Evaluate for malaria.
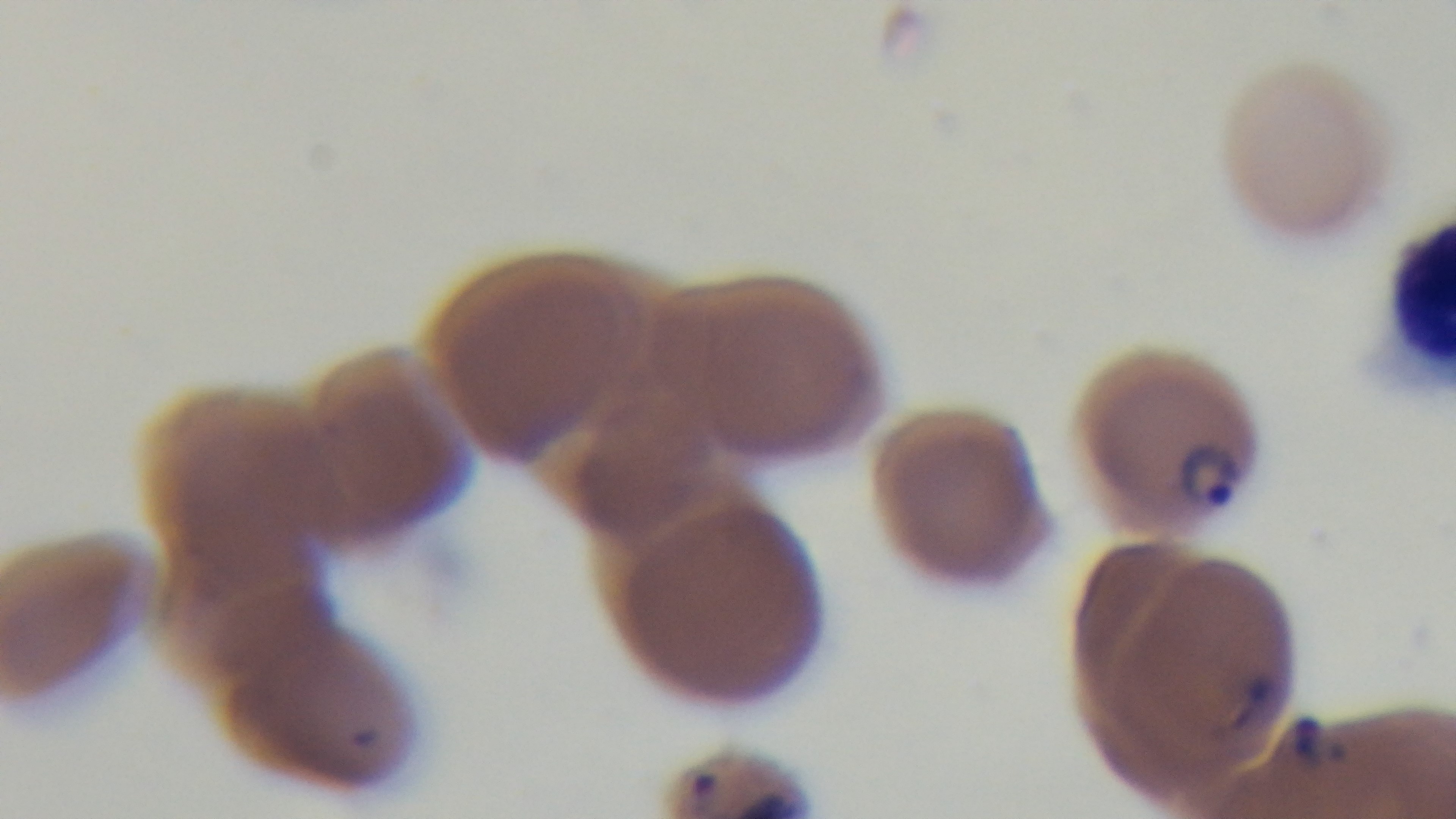

Infected.

Mounted 4K digital camera. Single field of view. Light microscopy. Oil-immersion objective, 100x. Preparation: thin blood film. Giemsa stain.